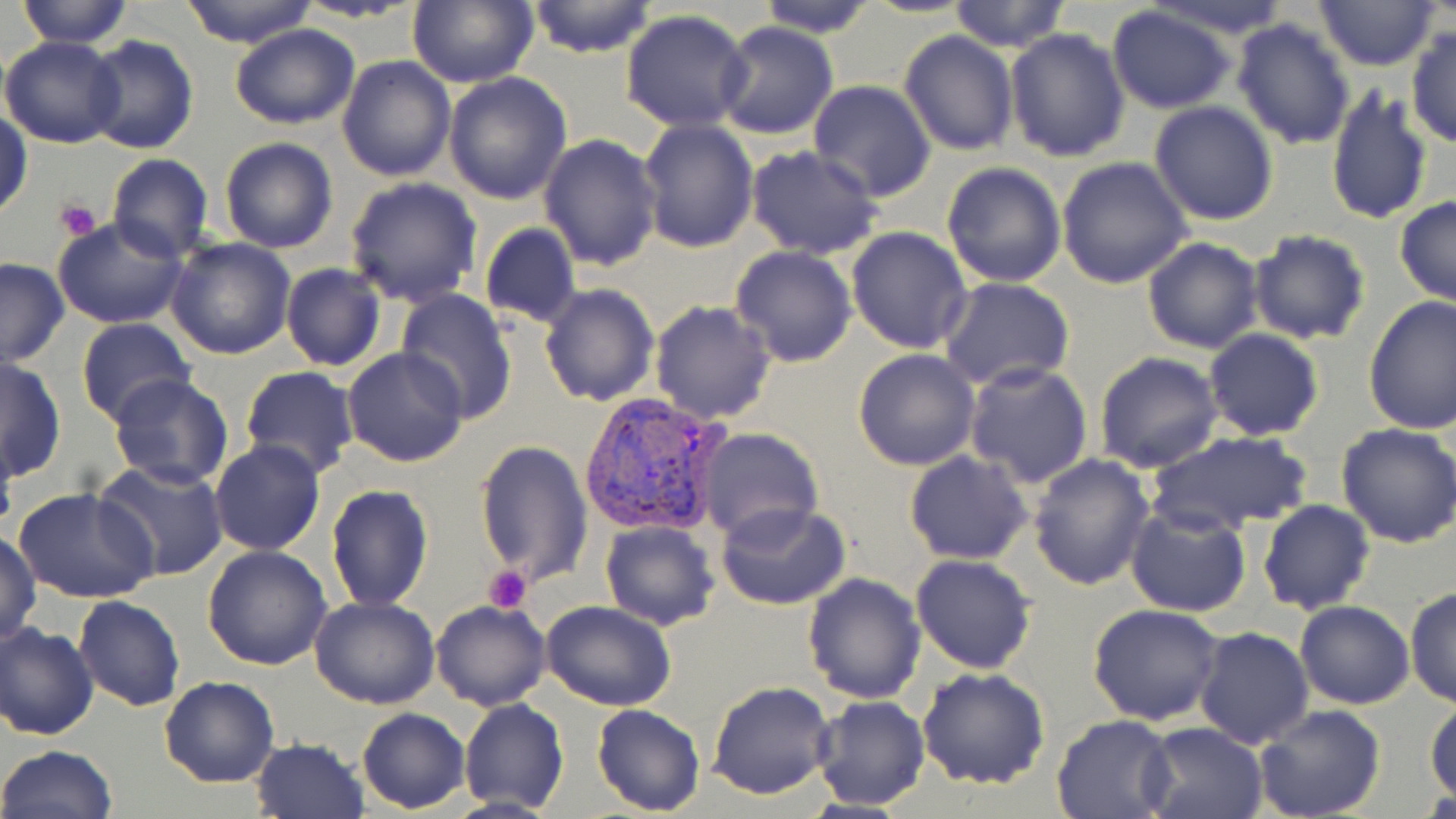

slide-level diagnosis = Plasmodium vivax
platelet locations = approximate bounding boxes as [x1, y1, x2, y2] in pixels: [55, 199, 100, 242], [483, 564, 534, 613]
modality = optical microscopy
stain = May-Grünwald-Giemsa
Plasmodium vivax-infected red blood cell locations = approximate bounding boxes as [x1, y1, x2, y2] in pixels: [578, 391, 729, 538]
uninfected red blood cell locations = approximate bounding boxes as [x1, y1, x2, y2] in pixels: [17, 0, 134, 47], [176, 0, 319, 47], [288, 0, 429, 24], [523, 0, 659, 58], [753, 0, 880, 37], [861, 0, 978, 18], [946, 0, 1072, 53], [1141, 0, 1296, 38], [1312, 0, 1442, 70], [403, 1, 540, 88], [1105, 5, 1238, 112], [620, 9, 753, 132], [1231, 17, 1357, 150], [714, 21, 838, 140], [229, 23, 361, 130], [1406, 26, 1455, 149], [1005, 28, 1131, 162], [899, 31, 1020, 158], [82, 35, 199, 155], [1, 36, 126, 148], [336, 55, 456, 182], [442, 73, 573, 205], [807, 81, 936, 201], [1325, 83, 1433, 227], [1148, 100, 1279, 225], [1, 110, 33, 219], [637, 119, 759, 252], [538, 132, 663, 270], [218, 138, 339, 255], [746, 145, 882, 259], [106, 154, 213, 262], [1056, 157, 1194, 289], [941, 161, 1067, 287], [345, 176, 483, 306], [1394, 196, 1456, 307], [52, 218, 189, 329], [479, 223, 581, 328], [847, 226, 974, 354], [1247, 230, 1370, 346], [165, 237, 296, 360], [1141, 237, 1265, 354], [730, 246, 857, 367], [0, 258, 70, 368], [280, 263, 385, 370], [939, 275, 1074, 392], [538, 282, 661, 406], [394, 288, 518, 424], [1362, 295, 1456, 434], [651, 299, 778, 423], [75, 318, 197, 425], [1203, 329, 1326, 440], [342, 345, 469, 467], [852, 348, 981, 470], [1094, 352, 1223, 474], [0, 356, 66, 484], [964, 362, 1094, 487], [239, 366, 359, 481], [108, 373, 235, 491], [1335, 422, 1456, 548], [695, 427, 823, 544], [1147, 429, 1311, 538], [209, 438, 326, 556], [474, 439, 592, 588], [905, 450, 1034, 564], [1027, 454, 1155, 591], [94, 460, 230, 580], [325, 484, 435, 612], [15, 488, 158, 604], [715, 500, 850, 610], [1258, 500, 1375, 616], [1125, 506, 1252, 617], [600, 520, 720, 632], [1, 530, 41, 647], [203, 544, 332, 669], [911, 555, 1038, 674], [802, 573, 929, 704], [1404, 586, 1455, 707], [309, 595, 441, 710], [74, 596, 186, 711], [430, 600, 551, 712], [541, 600, 677, 712], [1295, 600, 1415, 710], [1087, 603, 1225, 725], [0, 622, 99, 740], [1193, 627, 1314, 748], [918, 667, 1052, 789], [158, 677, 280, 788], [708, 681, 836, 800], [809, 695, 929, 811], [1424, 695, 1456, 803], [458, 698, 568, 815], [592, 704, 707, 816], [1255, 704, 1387, 819], [356, 709, 470, 812], [1051, 714, 1178, 819], [1141, 722, 1269, 819], [250, 737, 369, 818], [0, 745, 118, 819]
magnification = 1000x
image size = 1456×819 pixels
field of view = one of a larger specimen
preparation = thin blood smear